Outline each blood parasite and name the species.
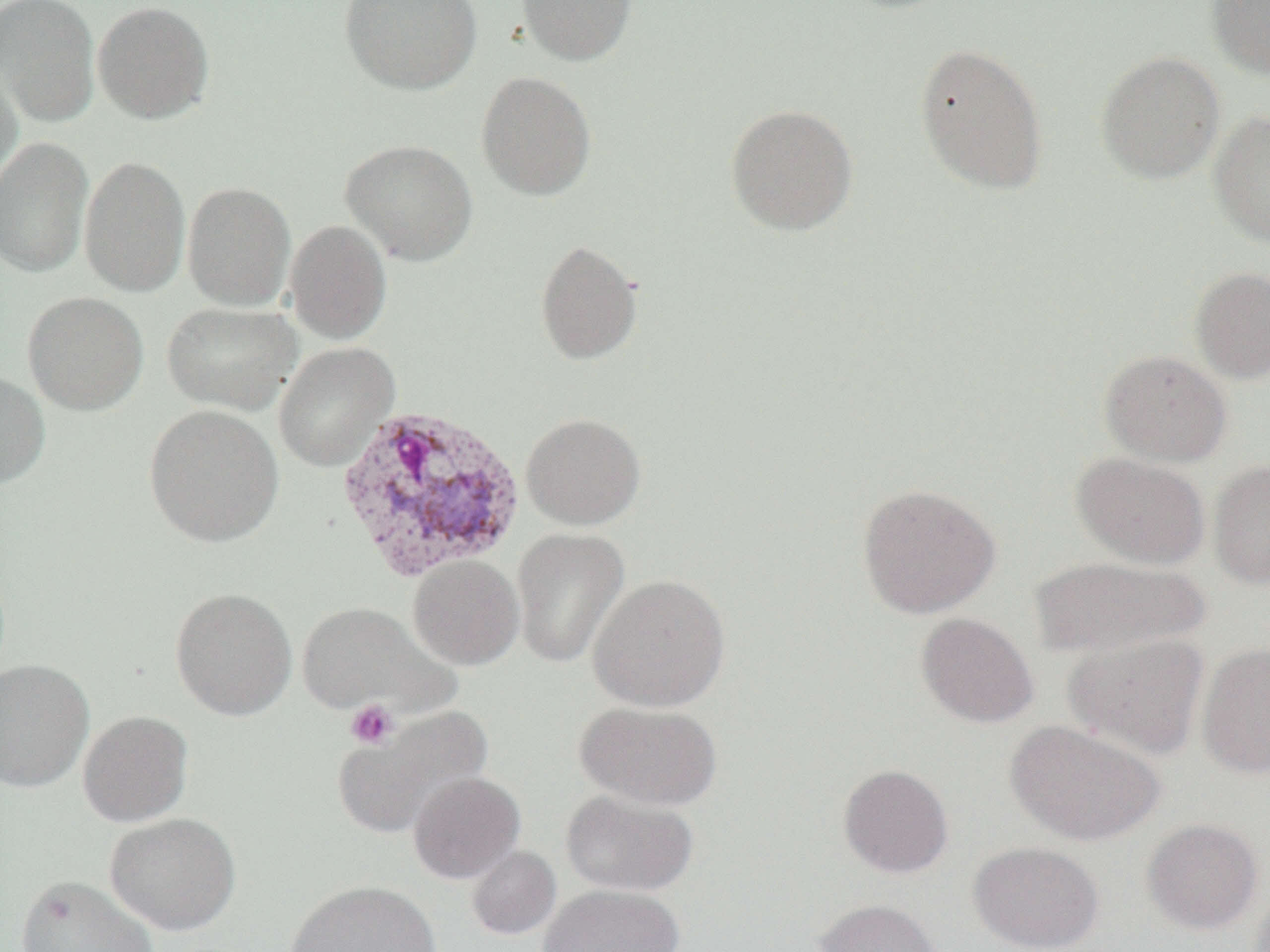

Approximate bounding boxes as named x1/y1/x2/y2 corners in pixels.
Plasmodium vivax-infected red blood cells: (x1=333, y1=402, x2=528, y2=583).
No Plasmodium falciparum, Plasmodium ovale, Plasmodium malariae, Babesia divergens, or Trypanosoma brucei observed.

Platelet locations: (x1=345, y1=699, x2=399, y2=749). Uninfected red blood cell locations: (x1=0, y1=0, x2=100, y2=127), (x1=340, y1=0, x2=482, y2=94), (x1=516, y1=0, x2=637, y2=66), (x1=831, y1=0, x2=961, y2=14), (x1=1206, y1=0, x2=1270, y2=79), (x1=92, y1=1, x2=215, y2=124), (x1=914, y1=42, x2=1049, y2=195), (x1=1094, y1=50, x2=1225, y2=185), (x1=0, y1=53, x2=23, y2=189), (x1=476, y1=71, x2=597, y2=201), (x1=724, y1=103, x2=859, y2=236), (x1=1208, y1=110, x2=1270, y2=247), (x1=0, y1=137, x2=94, y2=279), (x1=340, y1=139, x2=478, y2=266), (x1=79, y1=154, x2=191, y2=298), (x1=182, y1=182, x2=296, y2=312), (x1=284, y1=220, x2=392, y2=345), (x1=535, y1=239, x2=643, y2=365), (x1=1189, y1=267, x2=1270, y2=384), (x1=22, y1=291, x2=149, y2=414), (x1=162, y1=301, x2=302, y2=415), (x1=273, y1=342, x2=399, y2=472), (x1=1098, y1=350, x2=1232, y2=466), (x1=0, y1=369, x2=50, y2=491), (x1=143, y1=405, x2=284, y2=547), (x1=521, y1=413, x2=646, y2=530), (x1=1071, y1=453, x2=1210, y2=569), (x1=1209, y1=460, x2=1270, y2=589), (x1=856, y1=483, x2=1000, y2=619), (x1=511, y1=528, x2=629, y2=669), (x1=408, y1=555, x2=524, y2=670), (x1=1029, y1=556, x2=1208, y2=659), (x1=588, y1=574, x2=732, y2=712), (x1=169, y1=587, x2=298, y2=720), (x1=296, y1=602, x2=456, y2=716), (x1=916, y1=612, x2=1039, y2=728), (x1=1063, y1=632, x2=1210, y2=760), (x1=1196, y1=642, x2=1270, y2=779), (x1=0, y1=659, x2=94, y2=793), (x1=574, y1=701, x2=723, y2=810), (x1=334, y1=706, x2=493, y2=838), (x1=77, y1=710, x2=193, y2=826), (x1=1004, y1=719, x2=1165, y2=846), (x1=838, y1=763, x2=953, y2=878), (x1=408, y1=772, x2=525, y2=883), (x1=560, y1=789, x2=699, y2=896), (x1=104, y1=812, x2=241, y2=936), (x1=1141, y1=818, x2=1264, y2=934), (x1=968, y1=841, x2=1104, y2=951), (x1=466, y1=845, x2=561, y2=940), (x1=16, y1=874, x2=159, y2=952), (x1=286, y1=880, x2=440, y2=952), (x1=1248, y1=882, x2=1270, y2=952), (x1=538, y1=883, x2=685, y2=952), (x1=812, y1=898, x2=945, y2=952). Slide-level diagnosis: Plasmodium vivax. Image is 1270×952 pixels. One field of a larger specimen. Thin blood film. Captured at 1000x magnification. Optical microscopy.